Classify this cell by malaria status.
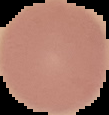

Uninfected.

Summary:
  - Image size: 109×115 pixels
  - Image type: cell region segmented out of the field of view; surrounding area masked to black
  - Preparation: thin blood smear